Report the malaria status of this cell.
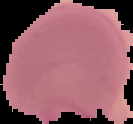
It is parasitized.

From a thin blood film. Image is 133×124 pixels. Cell region segmented out of the field of view; the surrounding area is masked to black.